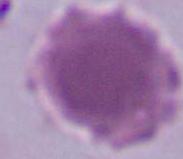

Micrograph. 1000x magnification. An erythrocyte is shown.